Give the preparation type.
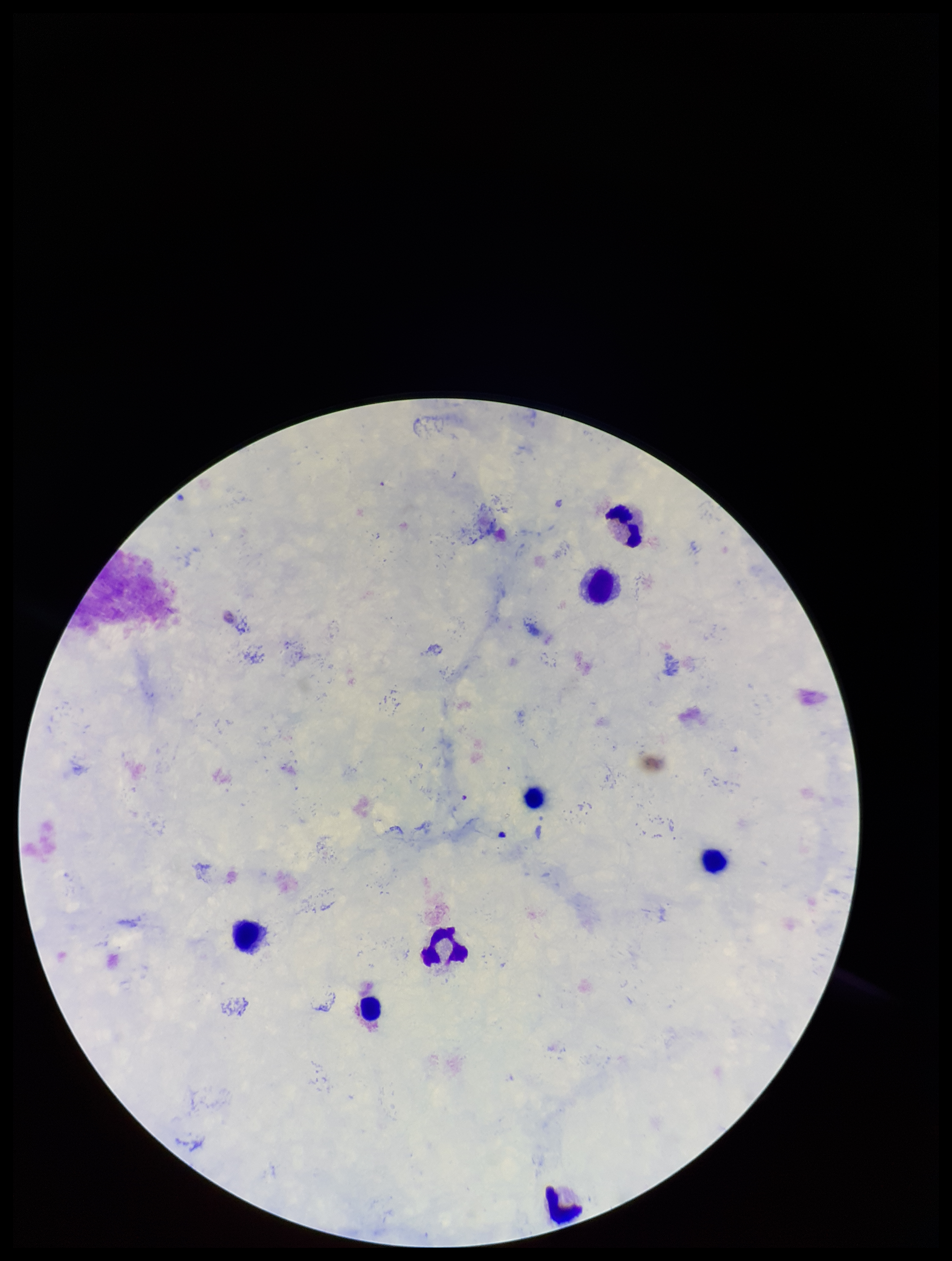

A thick smear.

Summary:
  - Image size: 952×1261 pixels
  - Parasite count: 0
  - Stain: Giemsa
  - Leukocyte count: 8
  - Patient malaria status: positive
  - Field of view: one from this slide
  - Plasmodium parasites: none seen
  - Species reported for this patient: Plasmodium falciparum
  - Capture: smartphone photograph through the microscope eyepiece